Assess this cell for malaria.
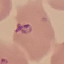

Parasitized.

Acquired by smartphone through the microscope eyepiece. Giemsa-stained preparation. Automatically extracted cell patch, resized to 64 × 64 pixels. Thin smear of blood.